State which parasite is depicted.
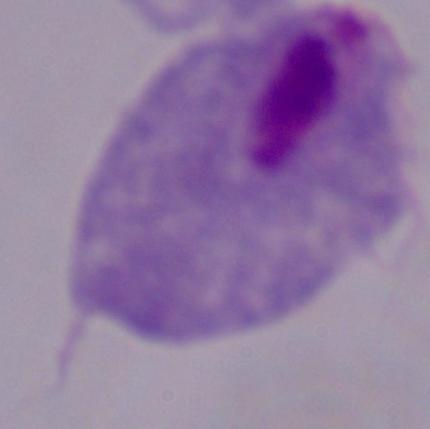
This is a trichomonad.

magnification = 1000x
modality = photomicrograph